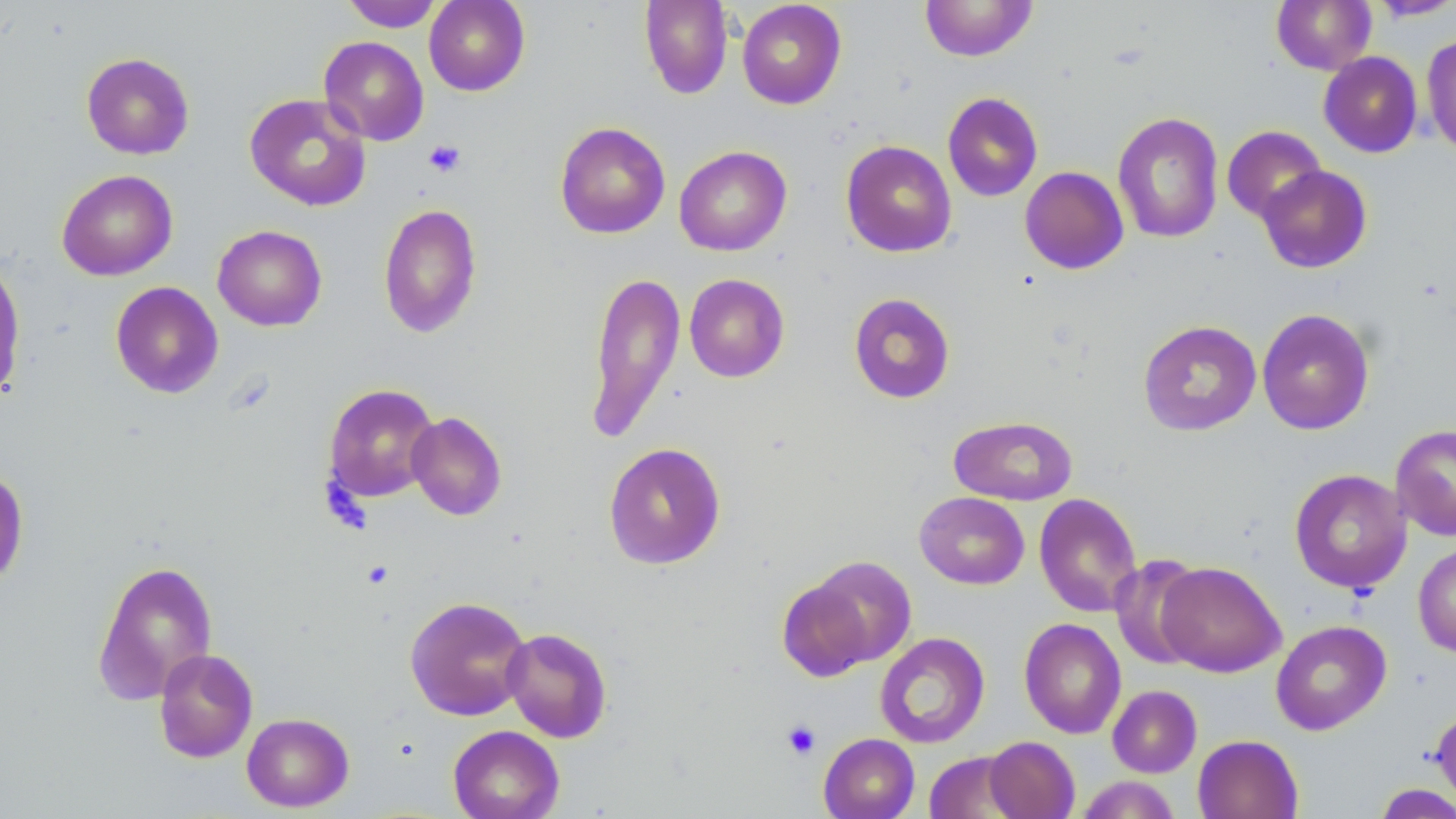 Approximate bounding boxes as [x1, y1, x2, y2] in pixels. Uninfected red blood cell locations: [340, 0, 446, 32], [424, 0, 530, 96], [639, 0, 733, 99], [1271, 0, 1376, 74], [1367, 0, 1456, 21], [737, 1, 847, 109], [919, 1, 1037, 61], [1421, 34, 1456, 157], [318, 36, 429, 145], [81, 52, 195, 160], [1318, 52, 1423, 158], [942, 92, 1043, 201], [244, 93, 371, 211], [1112, 112, 1224, 244], [555, 122, 670, 239], [1222, 125, 1326, 223], [841, 140, 957, 258], [674, 145, 792, 256], [1257, 165, 1372, 273], [1019, 166, 1128, 274], [56, 169, 178, 281], [378, 203, 482, 338], [212, 225, 327, 331], [0, 257, 26, 402], [584, 270, 686, 444], [684, 274, 790, 382], [110, 281, 224, 398], [848, 292, 956, 404], [1257, 307, 1375, 435], [1138, 320, 1261, 436], [323, 383, 440, 503], [406, 412, 507, 520], [947, 415, 1078, 506], [1390, 424, 1456, 541], [603, 442, 726, 569], [0, 466, 30, 588], [1289, 468, 1413, 594], [915, 491, 1029, 590], [1034, 493, 1143, 617], [1413, 543, 1456, 658], [1110, 555, 1207, 669], [800, 556, 918, 669], [92, 558, 218, 705], [1155, 561, 1286, 677], [775, 575, 881, 682], [404, 595, 532, 721], [1019, 617, 1126, 739], [1270, 619, 1392, 736], [501, 627, 613, 743], [875, 631, 990, 748], [154, 648, 258, 763], [1107, 685, 1202, 777], [1431, 707, 1456, 808], [241, 712, 355, 812], [447, 725, 564, 819], [818, 732, 920, 819], [1192, 734, 1304, 819], [984, 736, 1080, 819], [924, 751, 1025, 818], [1076, 776, 1181, 819], [1373, 783, 1456, 818]. Platelet locations: [423, 139, 466, 177], [782, 719, 820, 760]. Slide-level diagnosis: no evidence of blood parasites. Light microscopy. Thin blood film. Image is 1456×819 pixels. 1000x magnification. May-Grünwald-Giemsa stain. One field of a larger specimen.